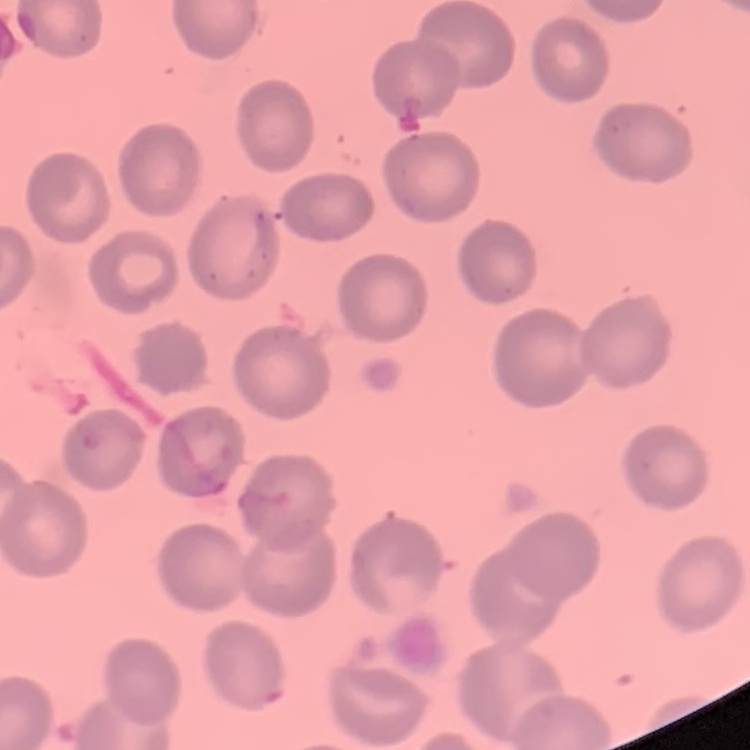

Summary:
  - Erythrocyte morphology: no rouleaux formation
  - Preparation: thin peripheral smear
  - Stain: Field's or Giemsa
  - Image type: one tile cut from a larger photomicrograph